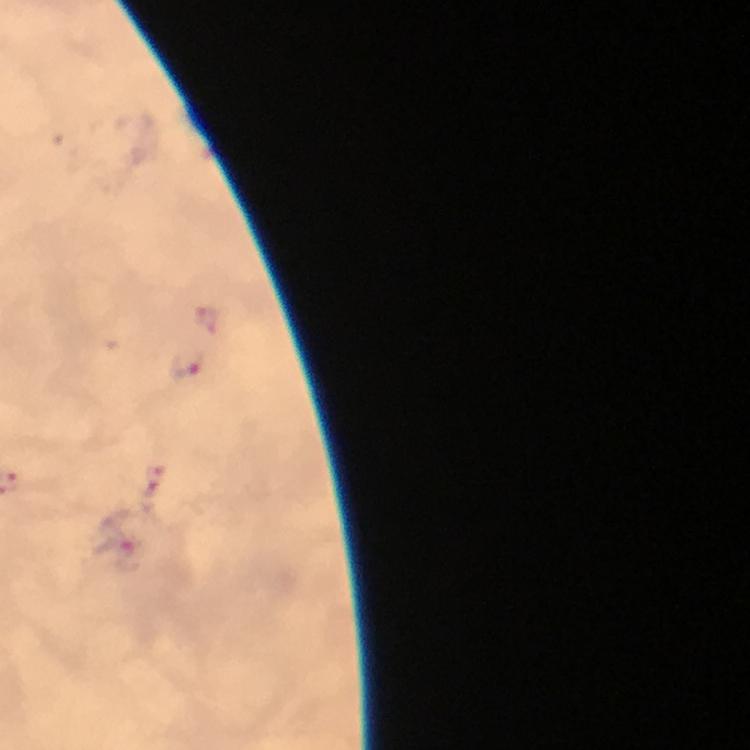 Approximate centers as {x, y} in pixels. Malaria parasite locations: {187, 366}, {151, 481}, {127, 555}. From a diagnostic examination for malaria. Thick blood film. At 100x magnification. A crop from one field of view. Immersion oil was used. Giemsa-stained preparation. Photographed with a smartphone mounted on the microscope. Image is 750×750 pixels.